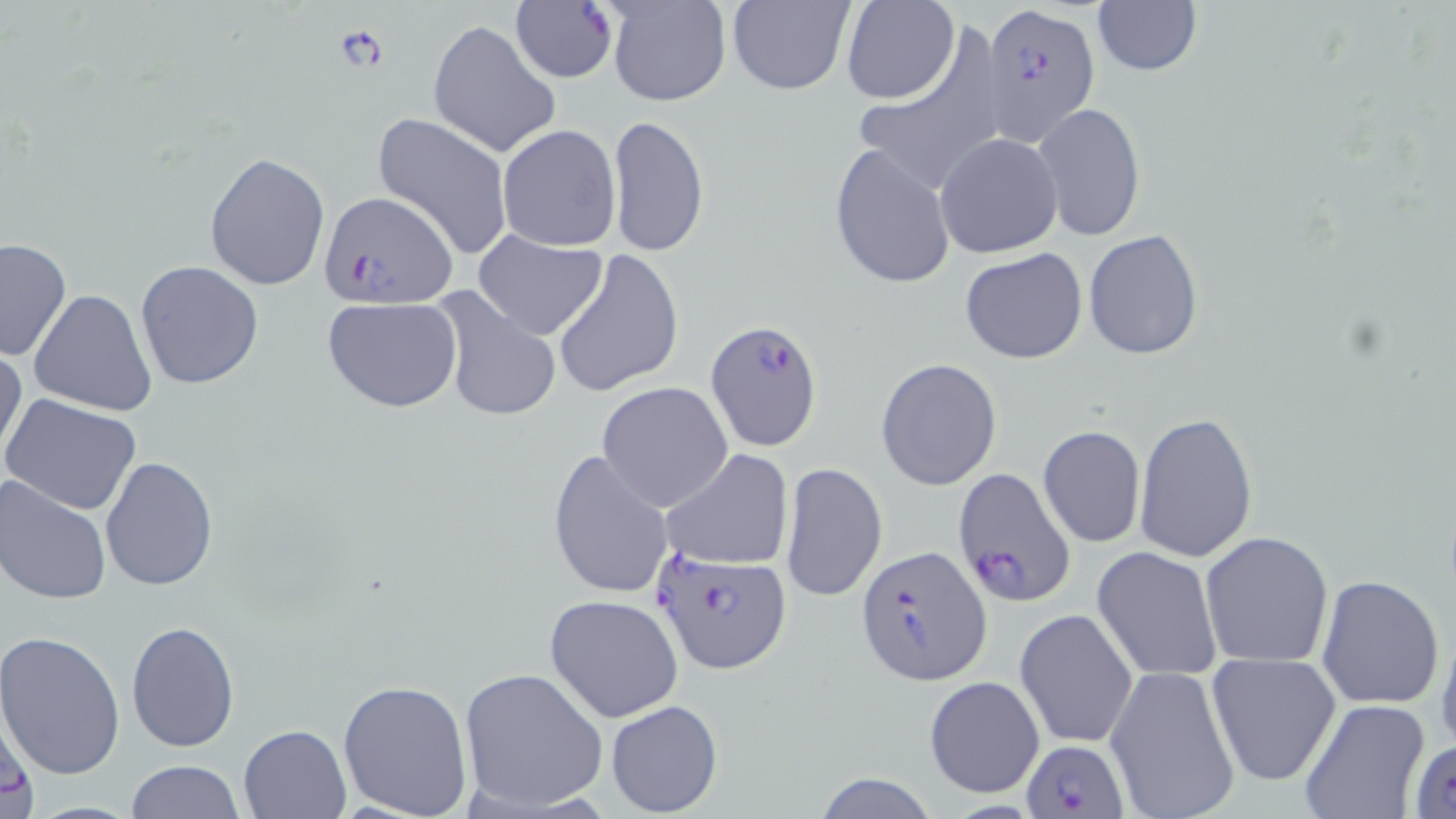
slide-level diagnosis = Plasmodium falciparum
modality = light microscopy
preparation = thin blood smear
uninfected red blood cell locations = approximate bounding boxes as (x1,y1)-(x2,y2) corner pairs in pixels: (606,0)-(731,106), (726,1)-(856,96), (839,1)-(959,106), (1090,2)-(1203,78), (428,18)-(560,160), (851,19)-(1012,198), (1032,104)-(1146,242), (370,113)-(515,260), (606,114)-(709,257), (496,124)-(621,251), (935,132)-(1063,258), (828,141)-(956,293), (203,152)-(330,291), (471,230)-(608,340), (1082,230)-(1203,359), (1,236)-(71,359), (959,246)-(1090,365), (551,247)-(685,398), (135,260)-(265,391), (29,288)-(157,417), (431,290)-(562,423), (322,296)-(463,413), (0,341)-(26,464), (876,358)-(1002,489), (596,382)-(733,512), (1,394)-(144,517), (1133,412)-(1257,563), (1038,425)-(1146,547), (661,449)-(792,571), (547,451)-(675,600), (99,456)-(219,592), (779,462)-(888,603), (0,476)-(112,606), (1199,532)-(1334,669), (1093,547)-(1222,681), (1315,572)-(1444,710), (544,594)-(684,723), (1015,608)-(1138,749), (1436,618)-(1456,756), (125,620)-(240,752), (0,632)-(125,778), (1206,654)-(1341,786), (1103,664)-(1241,819), (459,668)-(609,812), (924,674)-(1042,798), (338,679)-(474,818), (0,691)-(37,819), (605,699)-(724,816), (1300,699)-(1431,819), (239,723)-(353,818), (1408,739)-(1456,816), (125,760)-(244,817), (811,774)-(941,819)
Plasmodium falciparum-infected red blood cell locations = approximate bounding boxes as (x1,y1)-(x2,y2) corner pairs in pixels: (510,2)-(617,83), (982,2)-(1100,145), (317,193)-(458,308), (705,318)-(824,454), (948,465)-(1080,613), (857,544)-(992,686), (652,545)-(792,673), (1024,738)-(1125,817)
image size = 1456×819 pixels
magnification = 1000x
field of view = one of a larger specimen
stain = May-Grünwald-Giemsa